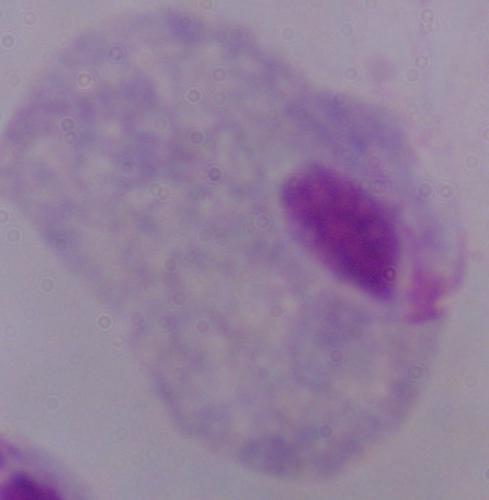

1000x magnification. A trichomonad is shown. Micrograph.